Report the malaria status of this cell.
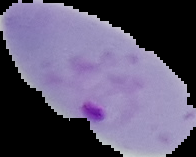

Parasitized.

{
  "preparation": "thin blood smear",
  "image_size": "196×157 pixels",
  "image_type": "cell region segmented out of the field of view; surrounding area masked to black"
}